Classify this cell by malaria status.
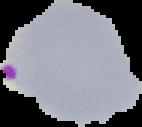

It is parasitized.

Summary:
  - Preparation: thin blood film
  - Image type: segmented cell region with the area outside set to black
  - Image size: 142×127 pixels